Describe the morphology of the red blood cells.
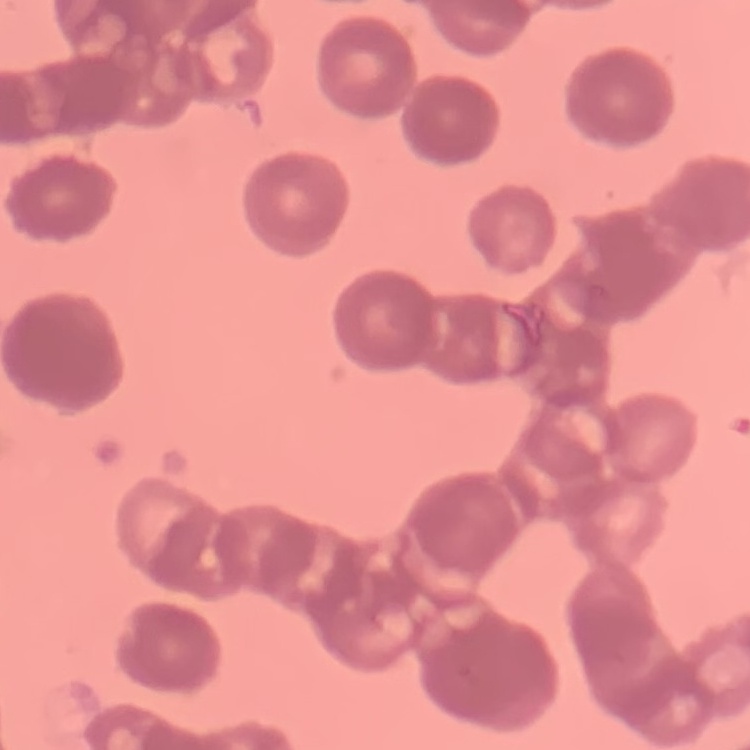

Rouleaux formation.

Summary:
  - Image type: square crop of a larger photomicrograph
  - Preparation: thin blood smear
  - Stain: Field's or Giemsa